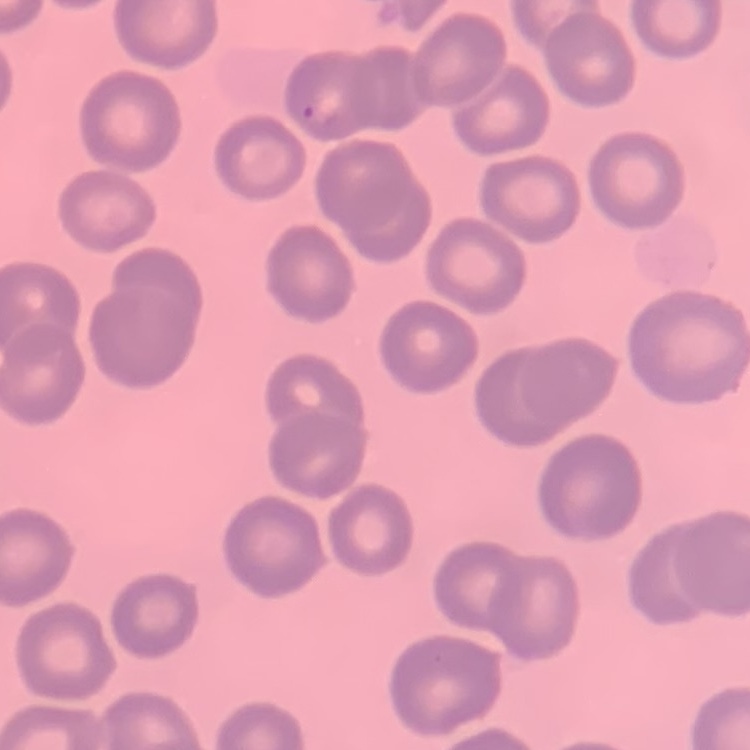
The erythrocytes show no rouleaux formation. Field's or Giemsa stain. One tile cut from a larger photomicrograph. Thin blood film.